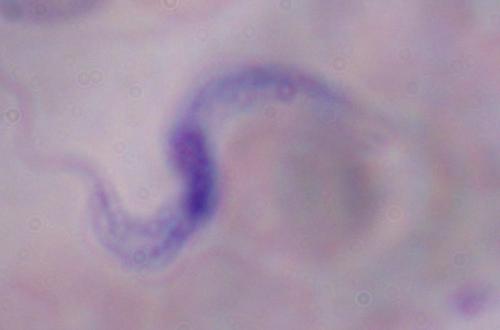
Photomicrograph. Captured at 1000x magnification. A trypanosome is seen.